Report the malaria status of this cell.
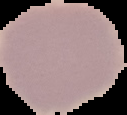
Uninfected.

image_type: cell region segmented out of the field of view; surrounding area masked to black
image_size: 127×115 pixels
preparation: thin blood smear